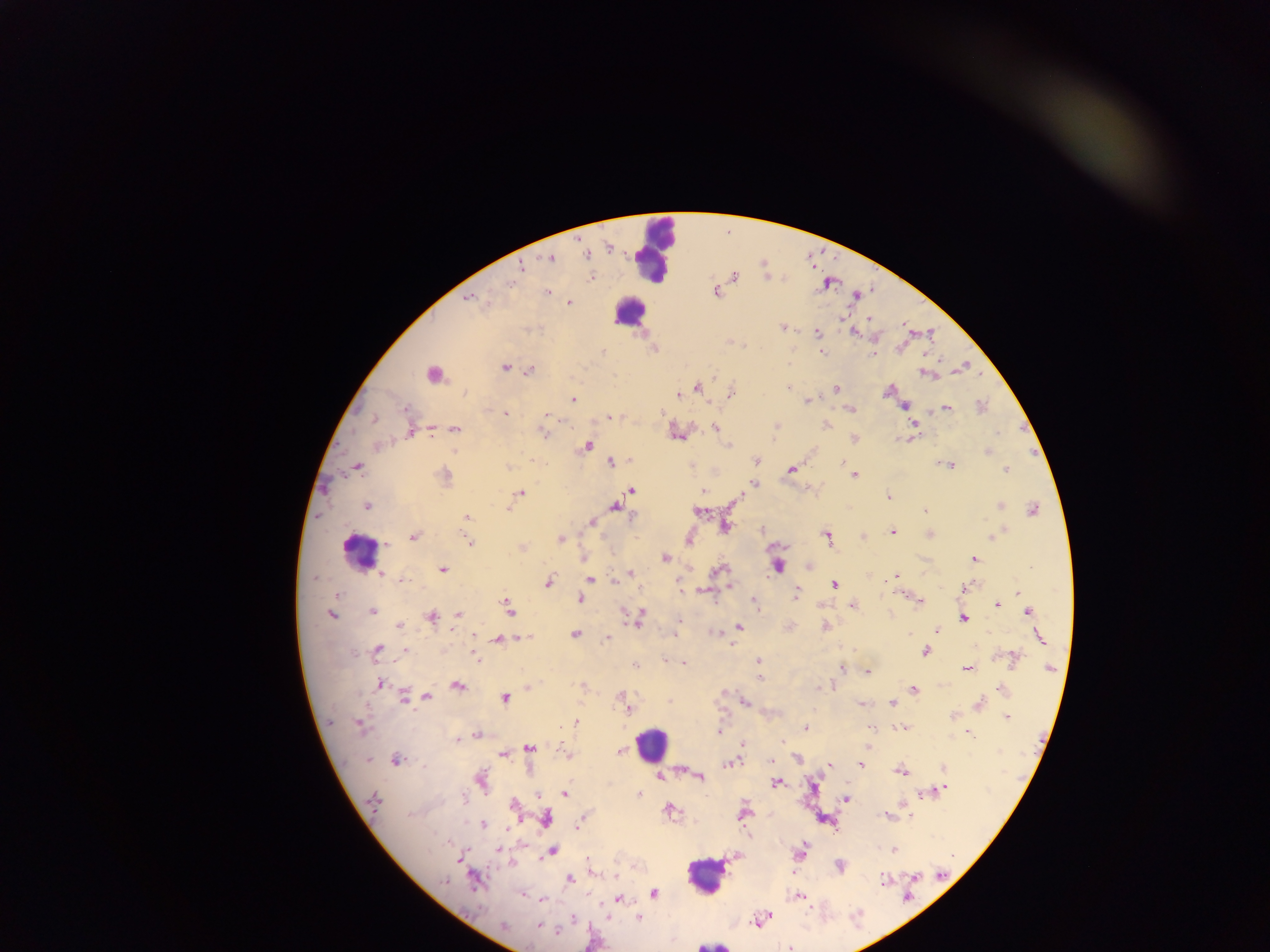

field of view = single
capture = mobile-phone photograph through a microscope
image size = 1270×952 pixels
malaria parasite locations = approximate centers as (x, y) in pixels: (609, 248), (551, 258), (521, 267), (734, 275), (591, 277), (510, 285), (547, 291), (716, 292), (856, 296), (470, 299), (570, 303), (870, 319), (782, 327), (817, 332), (853, 332), (820, 345), (602, 351), (822, 352), (873, 355), (504, 367), (529, 371), (432, 374), (714, 374), (926, 374), (787, 387), (697, 388), (835, 389), (887, 391), (731, 394), (678, 395), (573, 399), (808, 401), (905, 406), (981, 406), (947, 408), (851, 409), (405, 410), (662, 412), (506, 413), (547, 415), (609, 418), (373, 419), (826, 425), (914, 425), (715, 428), (456, 429), (411, 431), (543, 433), (998, 433), (678, 435), (854, 439), (728, 445), (586, 446), (988, 452), (757, 460), (534, 461), (610, 462), (843, 462), (950, 465), (508, 467), (357, 468), (791, 469), (1006, 470), (854, 475), (444, 476), (754, 484), (631, 490), (702, 491), (521, 494), (889, 496), (738, 498), (620, 502), (366, 506), (616, 506), (1000, 506), (509, 508), (924, 509), (1033, 510), (698, 511), (466, 517), (592, 522), (726, 526), (761, 529), (892, 532), (997, 533), (930, 534), (826, 536), (413, 537), (863, 537), (992, 537), (561, 539), (469, 541), (387, 545), (522, 547), (665, 558), (974, 559), (810, 564), (778, 566), (442, 569), (720, 570), (631, 573), (381, 574), (896, 576), (315, 578), (401, 579), (589, 579), (548, 582), (614, 582), (679, 585), (835, 585), (965, 588), (704, 590), (1018, 593), (337, 594), (796, 594), (580, 599), (919, 601), (755, 602), (853, 605), (997, 605), (508, 607), (372, 611), (1029, 612), (458, 614), (331, 615), (639, 616), (431, 617), (963, 618), (679, 621), (399, 625), (739, 627), (825, 627), (936, 631), (575, 634), (674, 634), (909, 635), (524, 637), (606, 638), (1040, 638), (497, 640), (378, 649), (405, 651), (925, 651), (476, 657), (1014, 659), (665, 661), (759, 661), (684, 663), (635, 667), (967, 668), (842, 669), (1049, 669), (867, 671), (760, 678), (380, 684), (458, 686), (582, 686), (528, 687), (821, 687), (914, 689), (1001, 689), (403, 697), (428, 697), (506, 698), (745, 701), (892, 703), (861, 704), (978, 705), (629, 709), (1006, 717), (576, 722), (360, 726), (872, 727), (904, 727), (805, 728), (718, 730), (968, 733), (476, 735), (457, 740), (782, 742), (742, 744), (529, 747), (619, 751), (502, 754), (567, 754), (797, 759), (368, 760), (396, 761), (771, 761), (730, 763), (829, 764), (861, 765), (943, 768), (900, 771), (660, 777), (700, 777), (481, 779), (777, 783), (814, 787), (943, 789), (565, 793), (639, 794), (923, 795), (462, 798), (847, 798), (373, 800), (513, 804), (670, 811), (744, 814), (886, 815), (545, 819), (582, 819), (580, 824), (482, 825), (577, 828), (507, 829), (894, 849), (499, 850), (801, 850), (552, 851), (459, 859), (589, 860), (840, 865), (615, 875), (916, 877), (570, 879), (884, 880), (445, 881), (474, 881), (654, 892), (523, 895), (799, 897), (543, 899), (618, 900), (574, 918), (639, 918), (760, 919), (503, 926), (538, 926), (558, 931), (789, 948)
leukocyte locations = approximate centers as (x, y) in pixels: (654, 249), (629, 311), (358, 552), (651, 743), (704, 875), (712, 945)
country = Ghana
preparation = thick blood film